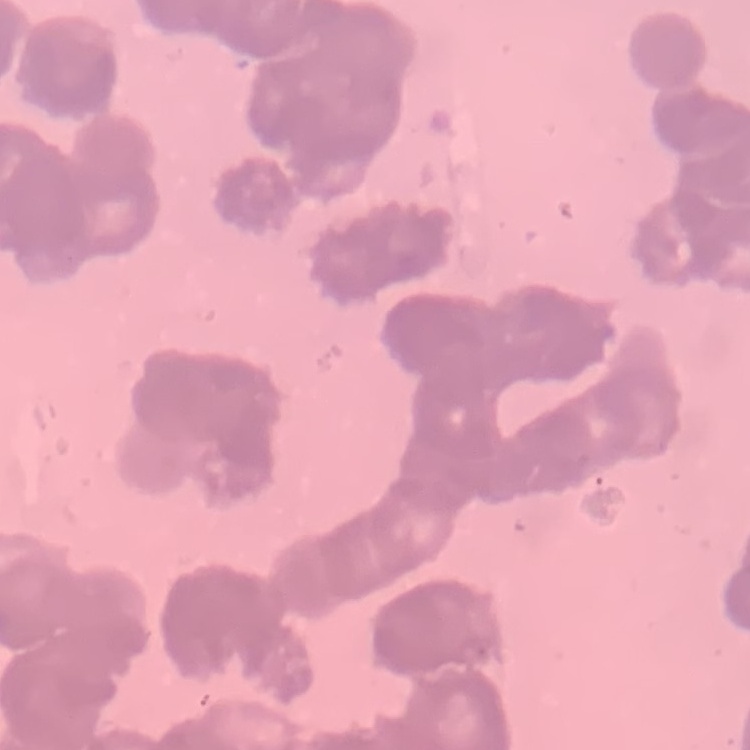 The red blood cells exhibit rouleaux formation. Stained with either Field's or Giemsa. Thin blood smear. Square crop of a larger photomicrograph.